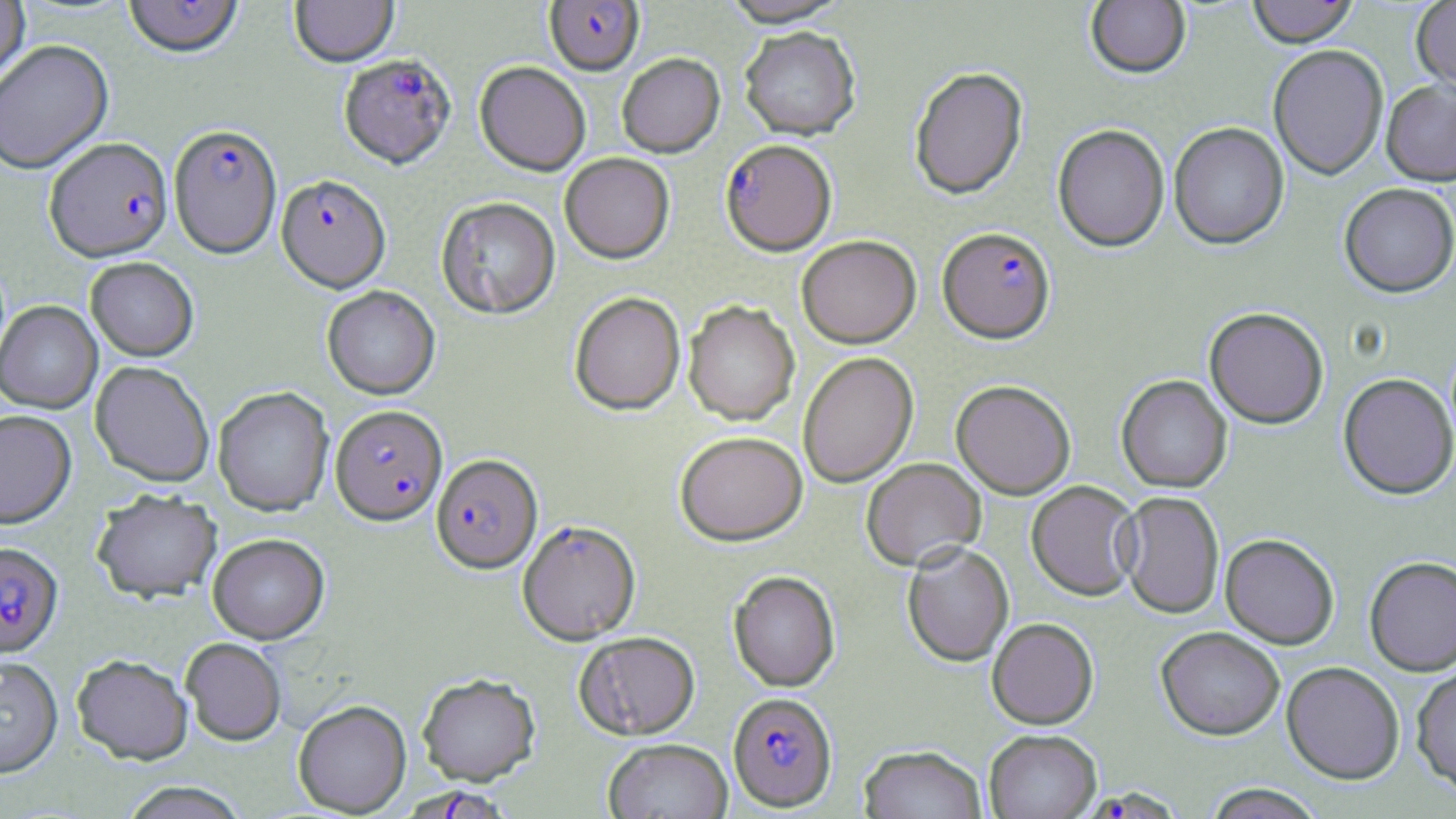
Approximate bounding boxes as [x1, y1, x2, y2] in pixels. Uninfected red blood cell locations: [0, 0, 31, 85], [123, 0, 244, 61], [290, 0, 399, 69], [719, 0, 852, 30], [1086, 0, 1191, 81], [1247, 0, 1360, 51], [1411, 0, 1456, 98], [739, 30, 861, 143], [1, 41, 114, 176], [1268, 47, 1388, 182], [617, 55, 725, 160], [474, 63, 590, 178], [910, 68, 1029, 202], [1381, 83, 1456, 189], [1169, 124, 1289, 252], [1052, 126, 1170, 255], [560, 155, 675, 265], [1338, 186, 1455, 301], [436, 198, 560, 320], [797, 237, 921, 350], [85, 258, 199, 362], [322, 287, 440, 401], [570, 293, 686, 416], [684, 301, 799, 427], [0, 302, 103, 414], [1204, 310, 1328, 431], [798, 353, 919, 489], [90, 362, 214, 489], [1338, 375, 1455, 502], [1116, 376, 1233, 494], [951, 383, 1076, 500], [213, 388, 333, 518], [0, 411, 77, 530], [675, 434, 808, 547], [861, 459, 986, 573], [1026, 481, 1141, 603], [91, 492, 222, 605], [1117, 492, 1224, 620], [517, 523, 641, 646], [208, 535, 330, 645], [1220, 536, 1339, 651], [902, 545, 1014, 669], [1364, 559, 1456, 678], [728, 571, 840, 693], [987, 620, 1098, 731], [1156, 629, 1284, 742], [574, 633, 700, 741], [181, 639, 286, 745], [73, 656, 192, 765], [0, 658, 63, 779], [1281, 664, 1404, 787], [1412, 665, 1456, 800], [417, 674, 541, 786], [293, 700, 411, 816], [984, 732, 1101, 819], [603, 740, 733, 819], [859, 746, 987, 819], [118, 782, 250, 819], [1203, 785, 1326, 819]. Plasmodium falciparum-infected red blood cell locations: [542, 0, 645, 79], [338, 56, 457, 171], [169, 126, 282, 261], [44, 139, 174, 264], [720, 142, 836, 258], [277, 176, 391, 295], [937, 229, 1056, 347], [331, 407, 447, 527], [431, 457, 543, 577], [0, 543, 63, 657], [728, 694, 838, 813], [1088, 779, 1190, 819], [397, 784, 514, 818]. Slide-level diagnosis: Plasmodium falciparum. Image is 1456×819 pixels. May-Grünwald-Giemsa stain. Thin blood film. Optical microscopy. Single field of view. 1000x magnification.